Give the position of every leukocyte visible.
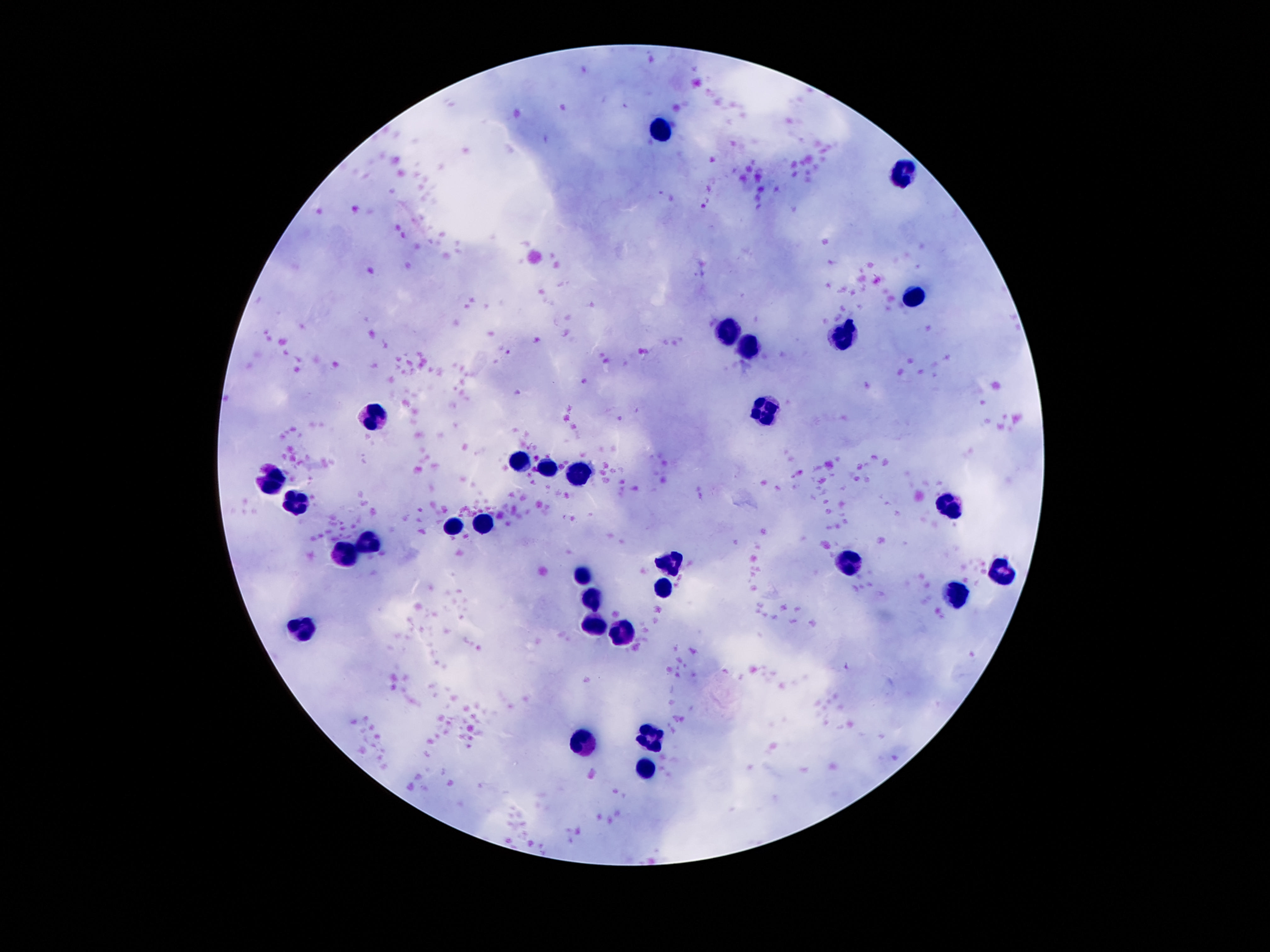
Approximate object centers, in pixels from the top-left corner.
Leukocytes: (x=658, y=127), (x=899, y=175), (x=912, y=298), (x=729, y=337), (x=844, y=337), (x=750, y=352), (x=763, y=409), (x=372, y=419), (x=521, y=463), (x=546, y=471), (x=576, y=471), (x=269, y=482), (x=297, y=505), (x=950, y=505), (x=483, y=524), (x=454, y=529), (x=368, y=541), (x=343, y=556), (x=670, y=561), (x=847, y=564), (x=1004, y=569), (x=584, y=573), (x=662, y=588), (x=590, y=594), (x=958, y=597), (x=591, y=620), (x=301, y=626), (x=624, y=633), (x=647, y=738), (x=582, y=744), (x=647, y=771).

Summary:
  - Field of view: one from this slide
  - Capture: smartphone camera through the microscope eyepiece
  - Preparation: thick blood film
  - Magnification: 100x
  - Stain: Giemsa
  - Patient malaria status: negative
  - Image size: 1270×952 pixels